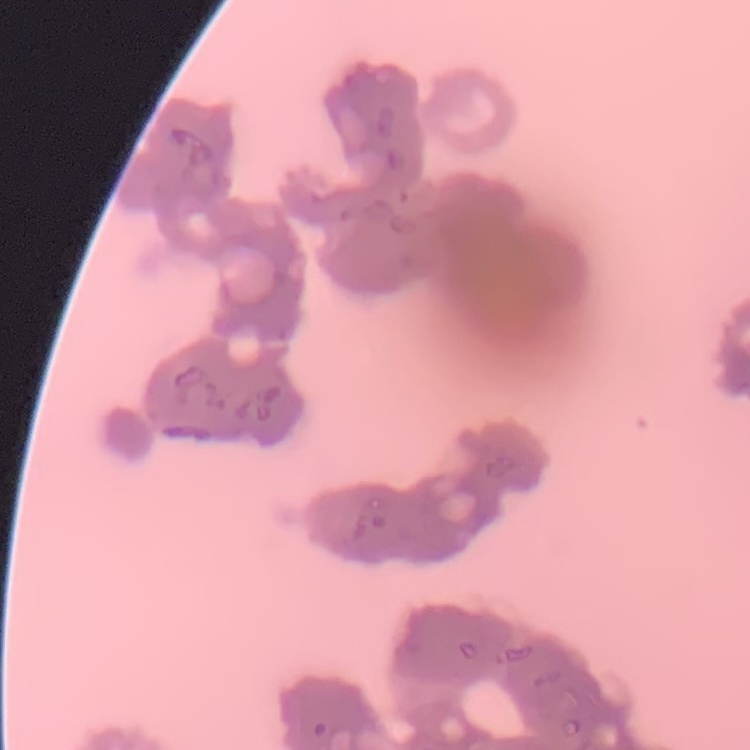

Summary:
  - Red blood cell morphology: rouleaux formation
  - Image type: square crop of a larger photomicrograph
  - Preparation: thin blood film
  - Stain: Field's or Giemsa